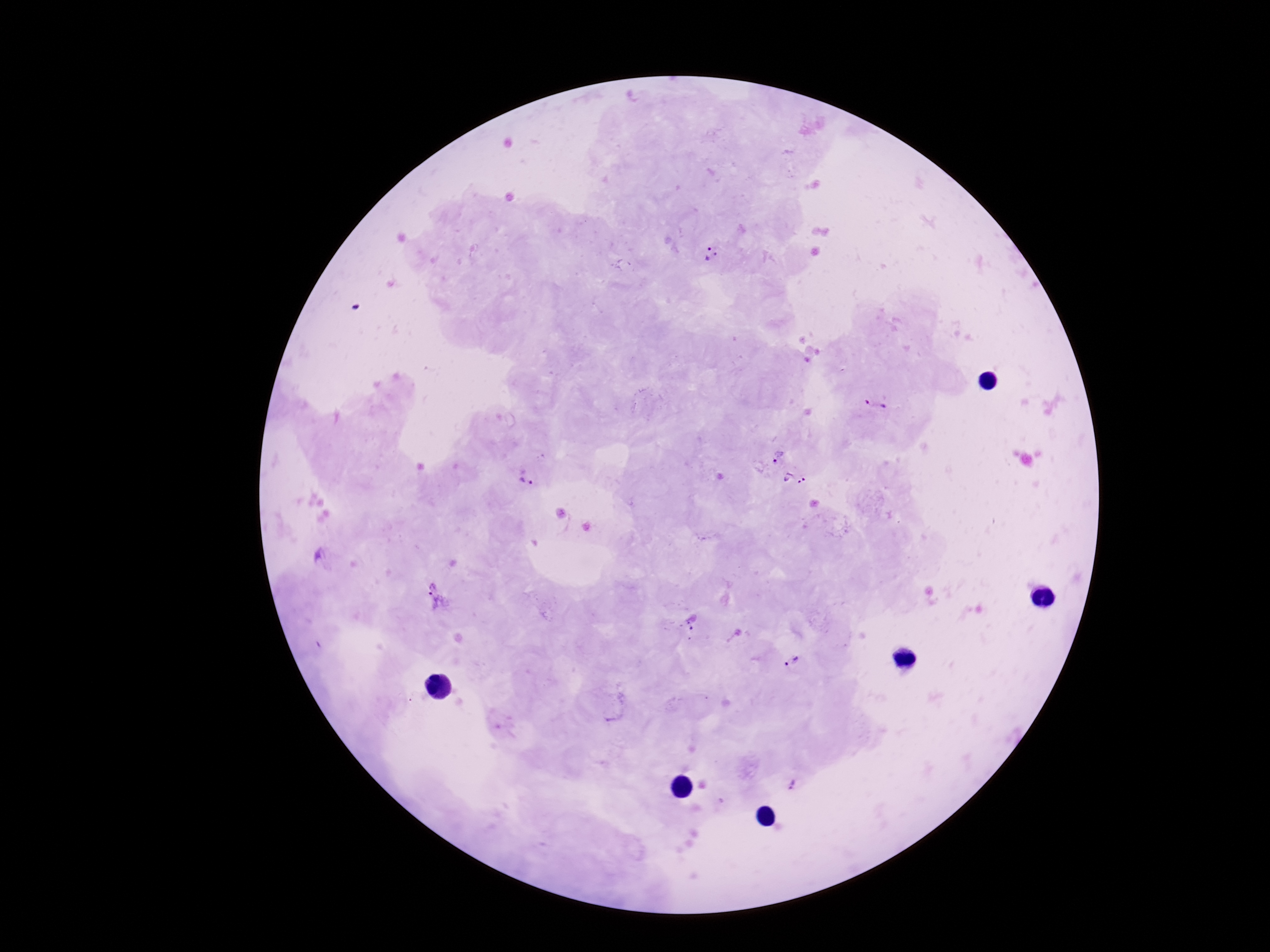
{
  "preparation": "thick blood film",
  "image_size": "1270×952 pixels",
  "stain": "Giemsa",
  "capture": "smartphone camera through the microscope eyepiece",
  "field_of_view": "single",
  "magnification": "100x",
  "plasmodium_parasite_locations": "approximate object centers, in pixels from the top-left corner: (x=711, y=254), (x=876, y=404), (x=778, y=455), (x=526, y=479), (x=795, y=479), (x=438, y=598), (x=692, y=621), (x=791, y=662), (x=793, y=785)",
  "patient_malaria_status": "positive"
}